Identify the blood parasite species.
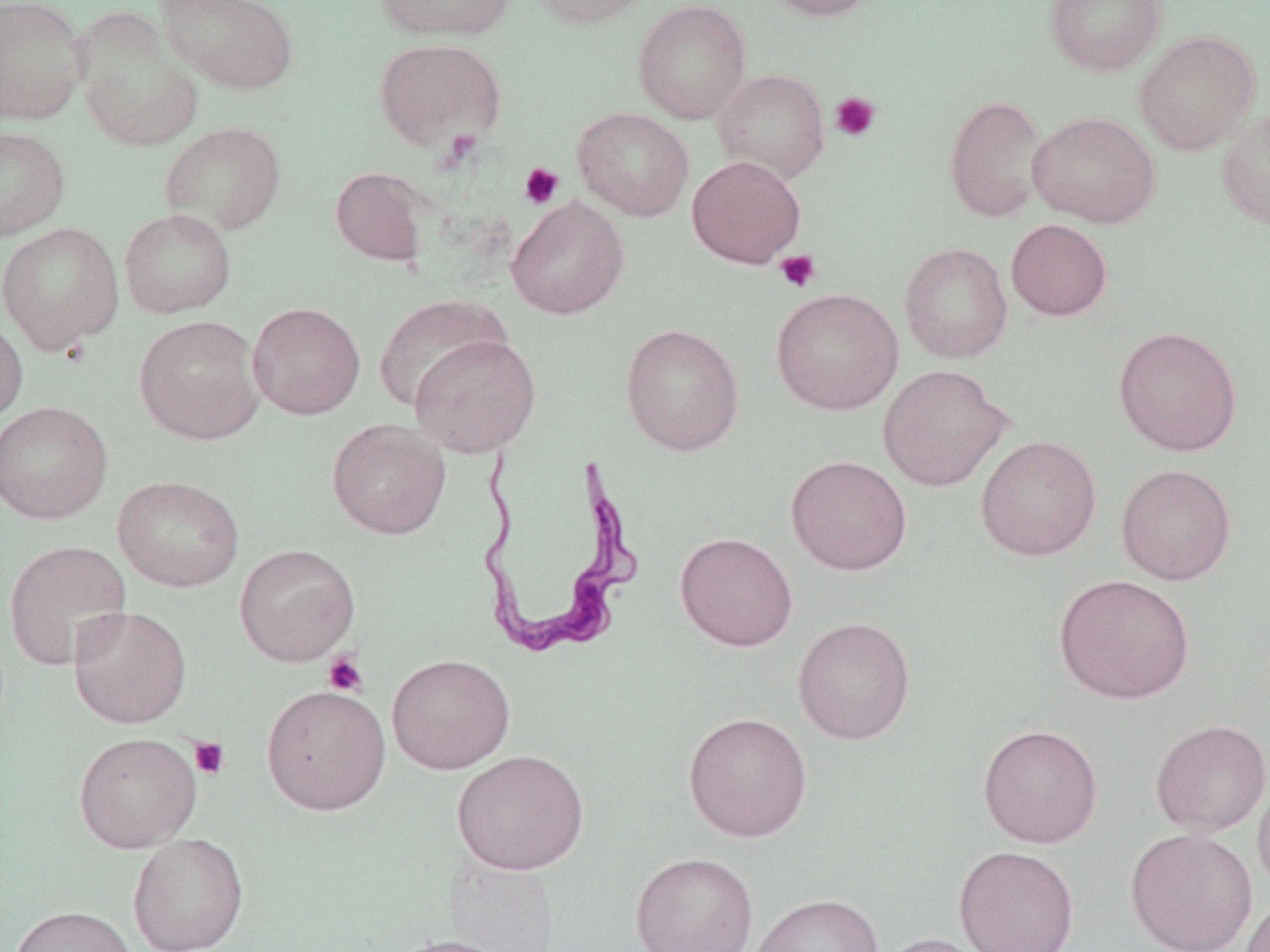
Trypanosoma brucei.

Approximate bounding boxes as [x1, y1, x2, y2] in pixels. Platelet locations: [830, 92, 881, 142], [519, 162, 564, 209], [775, 250, 822, 293], [323, 651, 368, 697], [190, 736, 229, 780]. Trypanosoma brucei locations: [472, 445, 642, 659]. Uninfected red blood cell locations: [0, 0, 90, 125], [157, 0, 299, 96], [375, 0, 516, 41], [528, 0, 657, 28], [633, 0, 751, 124], [765, 0, 880, 21], [1044, 0, 1167, 77], [76, 20, 204, 152], [1134, 31, 1259, 156], [373, 38, 507, 152], [711, 68, 830, 184], [944, 94, 1048, 223], [572, 107, 694, 221], [1216, 107, 1270, 231], [1028, 111, 1160, 228], [159, 121, 287, 236], [0, 125, 71, 242], [686, 155, 806, 268], [330, 167, 431, 267], [506, 196, 630, 320], [119, 208, 237, 319], [1006, 219, 1112, 321], [0, 222, 124, 354], [900, 242, 1013, 364], [770, 288, 904, 415], [373, 296, 510, 412], [246, 301, 365, 420], [0, 311, 28, 428], [134, 315, 265, 445], [621, 323, 744, 456], [1112, 325, 1243, 457], [408, 333, 541, 457], [877, 364, 1012, 492], [0, 400, 113, 524], [327, 419, 451, 539], [975, 435, 1102, 561], [786, 455, 913, 575], [1116, 463, 1236, 585], [112, 475, 245, 592], [675, 532, 798, 651], [3, 540, 133, 671], [234, 543, 360, 667], [1053, 574, 1194, 704], [68, 605, 192, 728], [793, 615, 916, 745], [386, 653, 516, 774], [261, 684, 391, 815], [683, 711, 813, 842], [1150, 719, 1270, 837], [978, 723, 1103, 848], [74, 732, 202, 853], [452, 749, 590, 875], [1253, 774, 1270, 896], [1124, 827, 1257, 952], [128, 833, 249, 952], [954, 845, 1080, 952], [630, 851, 759, 952], [749, 893, 885, 952], [1242, 894, 1270, 952], [10, 905, 139, 952], [876, 933, 994, 952], [382, 934, 519, 952]. Image is 1270×952 pixels. 1000x magnification. Thin blood film. Optical microscopy. Single field of view. May-Grünwald-Giemsa-stained preparation.